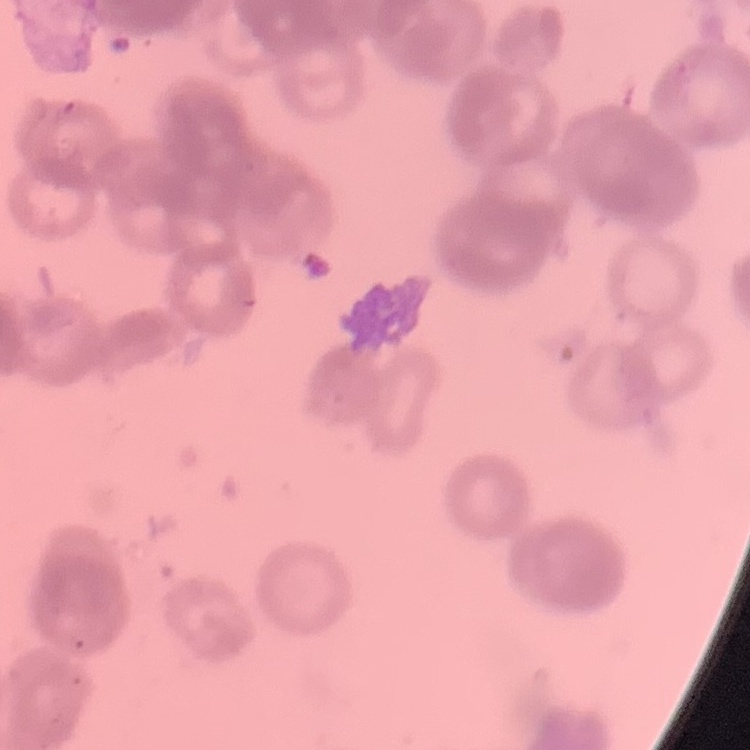

Summary:
  - Red blood cell morphology: rouleaux formation
  - Preparation: thin peripheral smear
  - Image type: one tile cut from a larger photomicrograph
  - Stain: Field's or Giemsa